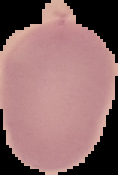

malaria_status: uninfected
image_size: 118×175 pixels
preparation: thin blood film
image_type: segmented cell region with the area outside set to black